Locate every blood parasite and identify its species.
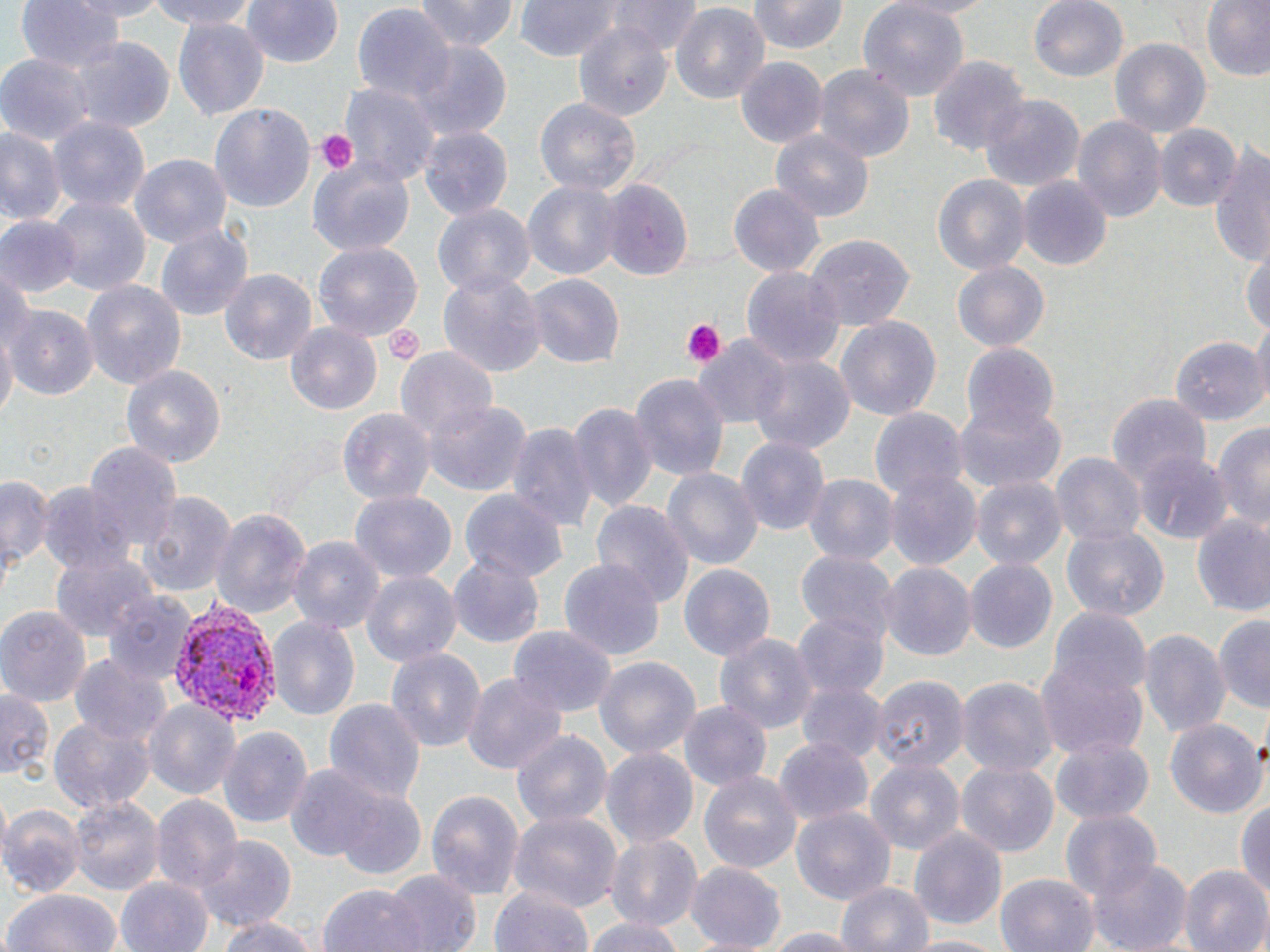
Approximate bounding boxes as (x1, y1, x2, y2) in pixels.
Plasmodium vivax-infected red blood cells: (169, 601, 282, 730).
No Plasmodium falciparum, Plasmodium ovale, Plasmodium malariae, Babesia divergens, or Trypanosoma brucei observed.

Summary:
  - Platelet locations: (316, 129, 360, 174), (681, 319, 726, 367), (382, 321, 425, 365)
  - Uninfected red blood cell locations: (15, 0, 126, 77), (58, 0, 177, 21), (139, 0, 265, 29), (239, 0, 345, 69), (417, 0, 518, 54), (513, 0, 625, 60), (610, 0, 703, 55), (749, 0, 847, 54), (857, 0, 968, 101), (885, 0, 1004, 19), (1028, 0, 1129, 83), (1201, 2, 1270, 82), (671, 4, 768, 106), (353, 5, 456, 106), (170, 17, 271, 121), (573, 25, 678, 119), (70, 36, 174, 134), (1111, 38, 1210, 139), (406, 43, 512, 140), (1, 53, 92, 143), (928, 55, 1029, 158), (736, 58, 828, 148), (815, 66, 912, 161), (341, 81, 438, 189), (980, 95, 1083, 191), (534, 97, 641, 197), (210, 104, 315, 211), (1073, 115, 1166, 226), (50, 118, 149, 218), (1154, 124, 1242, 212), (0, 127, 65, 229), (419, 127, 514, 221), (773, 128, 874, 220), (1208, 143, 1269, 267), (131, 154, 232, 251), (307, 157, 414, 255), (931, 172, 1031, 276), (1019, 175, 1113, 269), (597, 176, 692, 280), (522, 177, 623, 282), (730, 184, 824, 279), (50, 197, 149, 297), (432, 204, 534, 300), (0, 215, 80, 295), (155, 225, 252, 322), (803, 235, 914, 334), (315, 240, 424, 340), (1243, 245, 1270, 341), (954, 261, 1049, 354), (741, 265, 843, 369), (1, 268, 31, 360), (219, 269, 317, 366), (440, 272, 545, 378), (526, 274, 625, 369), (81, 278, 187, 390), (9, 306, 96, 399), (1253, 315, 1270, 413), (833, 316, 942, 423), (286, 323, 383, 415), (0, 328, 16, 426), (1171, 333, 1264, 425), (693, 334, 791, 426), (961, 345, 1059, 443), (394, 346, 498, 441), (748, 353, 854, 456), (121, 365, 226, 468), (630, 375, 729, 480), (1106, 394, 1213, 486), (423, 398, 533, 496), (569, 400, 658, 517), (952, 400, 1066, 494), (869, 406, 966, 503), (337, 407, 436, 505), (1213, 419, 1270, 535), (506, 422, 595, 537), (738, 436, 830, 539), (85, 440, 182, 552), (1136, 448, 1230, 544), (1052, 452, 1144, 551), (662, 467, 761, 574), (882, 468, 981, 573), (0, 472, 54, 575), (802, 474, 897, 569), (971, 476, 1065, 570), (39, 482, 137, 580), (460, 489, 566, 582), (136, 490, 237, 599), (350, 491, 457, 582), (593, 499, 692, 609), (210, 505, 311, 623), (1189, 510, 1270, 614), (1060, 523, 1170, 619), (289, 537, 384, 634), (50, 546, 155, 644), (796, 550, 898, 645), (449, 557, 543, 646), (560, 558, 663, 662), (964, 558, 1057, 653), (880, 562, 976, 663), (679, 563, 774, 663), (359, 571, 459, 668), (105, 590, 199, 687), (0, 607, 90, 704), (793, 609, 889, 700), (1049, 610, 1152, 705), (266, 615, 361, 720), (1214, 615, 1270, 713), (509, 625, 617, 716), (1139, 627, 1231, 738), (715, 633, 816, 735), (386, 646, 486, 754), (72, 652, 170, 745), (594, 654, 699, 762), (1036, 657, 1147, 760), (462, 670, 566, 778), (866, 673, 967, 773), (955, 675, 1057, 776), (797, 682, 883, 759), (1, 684, 54, 780), (323, 697, 426, 807), (143, 700, 239, 800), (678, 700, 771, 792), (49, 715, 153, 813), (1166, 719, 1265, 822), (217, 726, 312, 830), (511, 728, 612, 831), (773, 739, 872, 827), (1049, 740, 1155, 822), (600, 745, 699, 850), (864, 756, 965, 855), (956, 758, 1060, 854), (287, 764, 389, 866), (700, 771, 801, 875), (336, 786, 429, 878), (425, 789, 526, 902), (150, 793, 242, 895), (70, 796, 161, 893), (1236, 797, 1269, 902), (0, 804, 88, 894), (790, 805, 896, 905), (507, 809, 622, 915), (1057, 809, 1161, 908), (909, 826, 1008, 929), (605, 834, 702, 934), (194, 835, 296, 934), (1092, 856, 1193, 951), (684, 861, 787, 949), (1181, 865, 1270, 952), (382, 868, 479, 952), (995, 873, 1099, 952), (116, 874, 211, 952), (836, 879, 934, 952), (488, 881, 598, 952), (320, 882, 427, 952), (3, 889, 125, 952), (212, 913, 320, 952), (583, 915, 686, 952), (757, 926, 871, 950), (902, 933, 1006, 952)
  - Slide-level diagnosis: Plasmodium vivax
  - Preparation: thin blood smear
  - Field of view: single
  - Stain: May-Grünwald-Giemsa
  - Image size: 1270×952 pixels
  - Magnification: 1000x
  - Modality: light microscopy